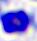

Summary:
  - Modality: micrograph
  - Magnification: 400x
  - Identification: leukocyte